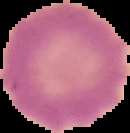
malaria_status: uninfected
image_size: 130×133 pixels
image_type: segmented cell region with the area outside set to black
preparation: thin blood film